Name the blood parasite species.
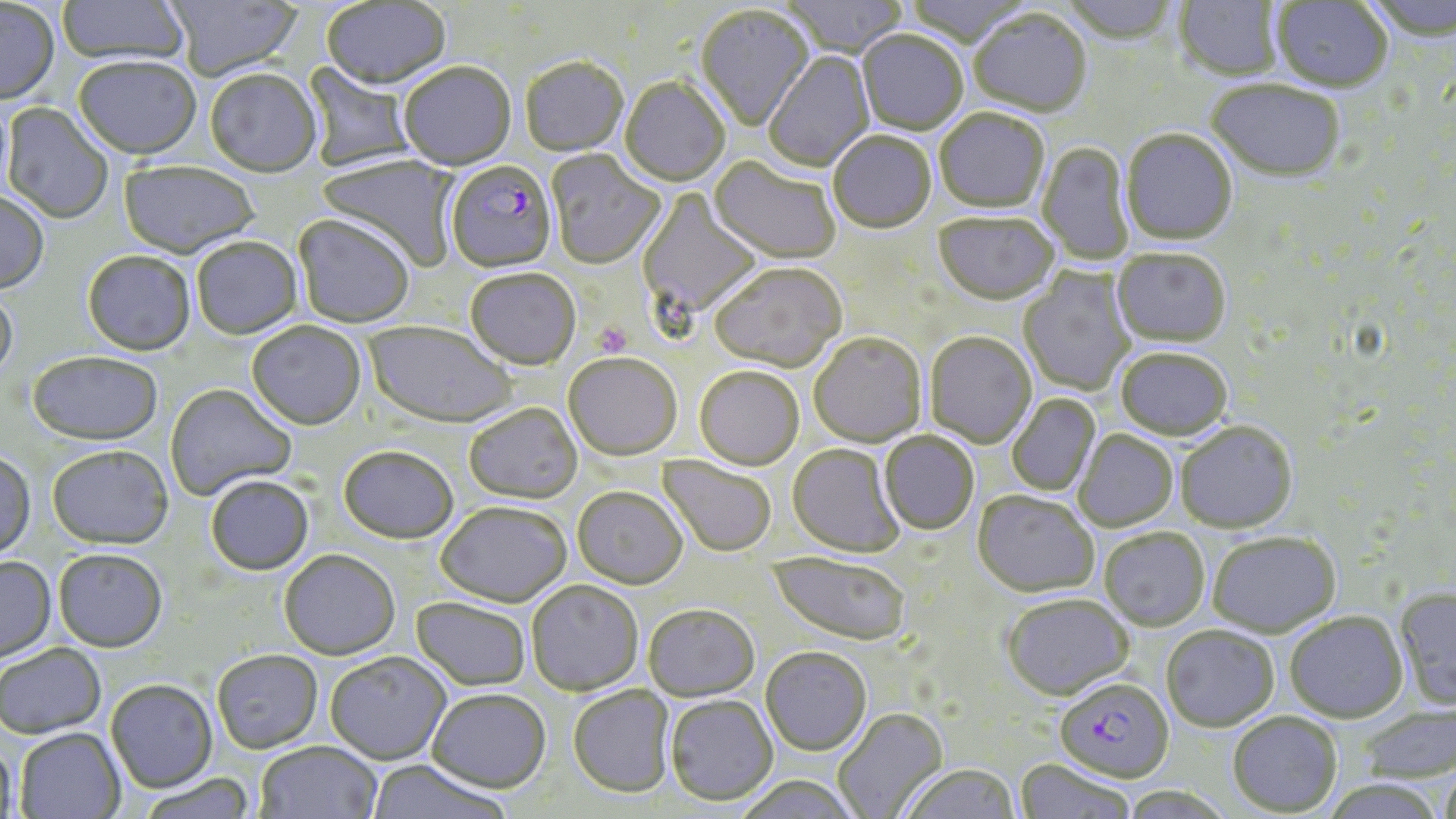

Plasmodium falciparum.

magnification = 1000x
stain = May-Grünwald-Giemsa
platelet locations = approximate bounding boxes as (x1,y1)-(x2,y2) corner pairs in pixels: (594,322)-(632,358)
image size = 1456×819 pixels
field of view = single
Plasmodium falciparum-infected red blood cell locations = approximate bounding boxes as (x1,y1)-(x2,y2) corner pairs in pixels: (445,163)-(557,275), (1055,678)-(1174,785)
preparation = thin blood film
uninfected red blood cell locations = approximate bounding boxes as (x1,y1)-(x2,y2) corner pairs in pixels: (57,0)-(190,68), (778,0)-(909,60), (903,0)-(1035,49), (1059,0)-(1180,46), (1175,0)-(1283,82), (1363,0)-(1455,43), (166,1)-(302,81), (322,1)-(451,93), (1271,1)-(1393,94), (0,3)-(60,106), (695,6)-(814,133), (969,11)-(1091,119), (856,32)-(968,136), (765,51)-(875,173), (73,59)-(202,162), (520,59)-(628,158), (301,61)-(419,172), (399,64)-(517,172), (204,71)-(322,180), (620,78)-(729,189), (1207,82)-(1345,185), (0,99)-(15,211), (2,103)-(113,224), (934,110)-(1049,215), (1121,131)-(1237,247), (828,133)-(936,236), (1037,142)-(1133,264), (546,151)-(666,270), (315,155)-(460,271), (709,157)-(840,266), (118,162)-(258,260), (637,188)-(763,322), (0,192)-(49,295), (933,215)-(1059,308), (293,216)-(415,329), (192,239)-(303,340), (1111,250)-(1231,349), (82,253)-(195,357), (710,265)-(847,374), (1018,267)-(1136,397), (465,270)-(580,373), (0,290)-(18,387), (247,322)-(366,432), (364,323)-(517,430), (924,333)-(1037,448), (809,334)-(927,448), (1116,349)-(1232,442), (27,353)-(164,446), (563,354)-(683,463), (694,368)-(804,471), (165,384)-(297,501), (1007,393)-(1100,497), (463,404)-(583,505), (1176,422)-(1298,535), (1074,430)-(1178,532), (879,433)-(979,536), (787,444)-(905,559), (47,446)-(174,550), (338,447)-(458,545), (0,451)-(36,562), (658,456)-(777,558), (205,477)-(314,576), (572,487)-(688,591), (972,492)-(1099,600), (436,504)-(572,609), (1100,528)-(1210,632), (1208,533)-(1341,639), (53,549)-(167,652), (279,551)-(400,660), (768,552)-(911,648), (0,557)-(56,663), (526,581)-(643,696), (1394,588)-(1456,709), (1001,596)-(1135,703), (410,597)-(531,691), (643,605)-(759,702), (1284,612)-(1407,723), (1161,626)-(1279,732), (0,644)-(107,739), (760,647)-(871,756), (212,650)-(323,753), (325,652)-(452,765), (106,681)-(217,793), (567,686)-(676,799), (426,689)-(551,794), (665,696)-(778,806), (833,708)-(948,819), (1228,713)-(1342,816), (15,728)-(125,819), (1,740)-(18,819), (256,742)-(383,819), (1014,760)-(1136,819), (365,761)-(511,819), (1439,765)-(1456,819), (901,766)-(1020,819), (138,774)-(257,819), (733,776)-(863,819), (1320,779)-(1448,819)
modality = optical microscopy